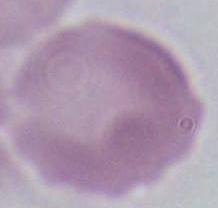
Summary:
  - Magnification: 1000x
  - Identification: red blood cell
  - Modality: micrograph